Report the malaria status of this cell.
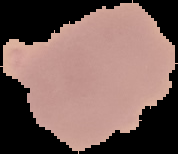

It is uninfected.

preparation = thin blood smear
image size = 178×154 pixels
image type = cell region segmented out of the field of view; surrounding area masked to black